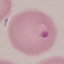
Result: malaria parasites identified. Giemsa stain. Acquired by smartphone through the microscope eyepiece. Thin blood film. Cell patch, automatically extracted from a larger field of view and resized to 64 × 64 pixels.